Assess this cell for malaria.
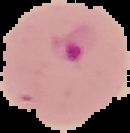

It is parasitized.

{
  "image_type": "segmented cell region on a black background",
  "image_size": "130×133 pixels",
  "preparation": "thin blood film"
}